Locate every blood parasite and identify its species.
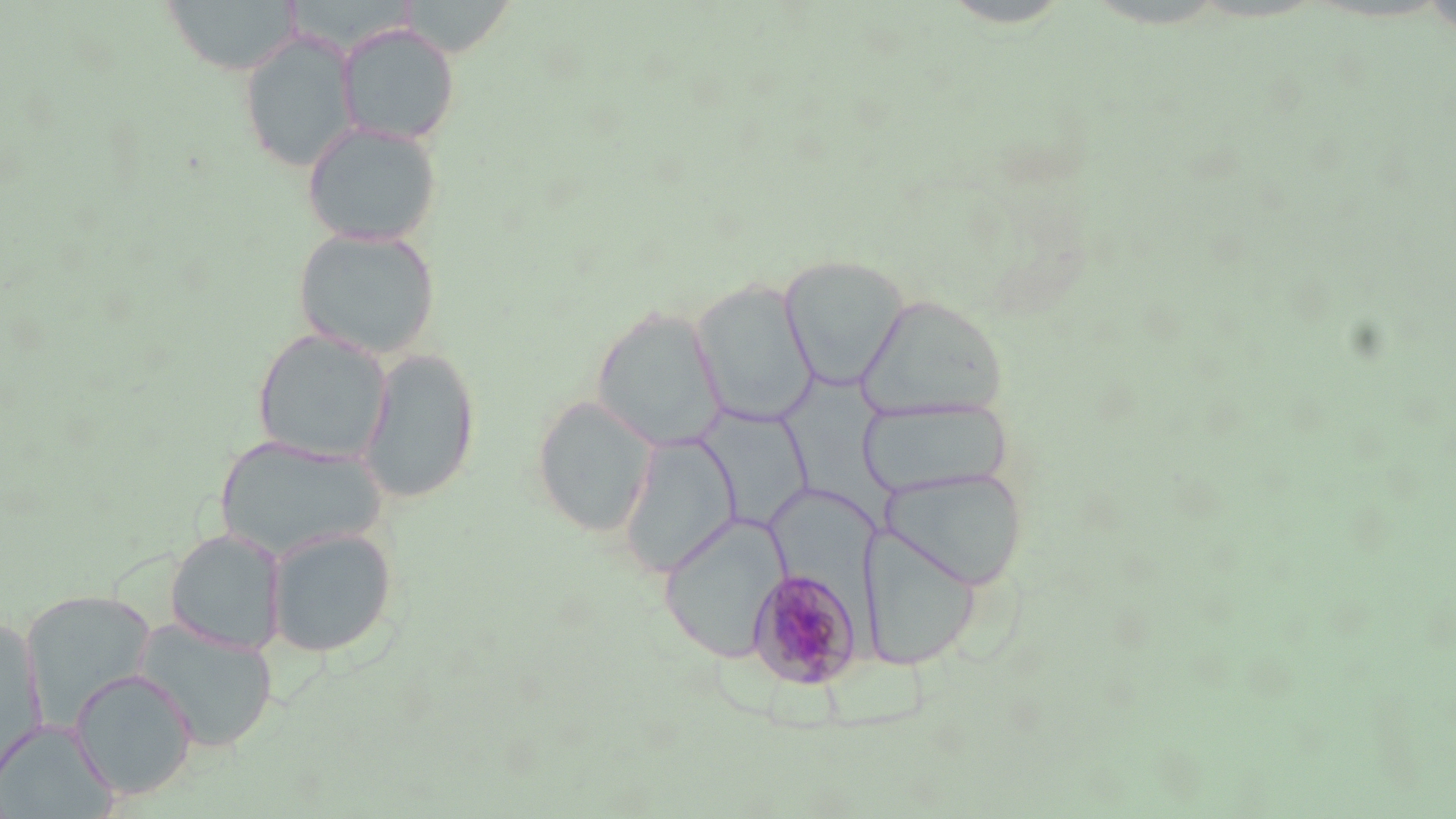
Approximate bounding boxes as (x1, y1, x2, y2) in pixels.
Plasmodium malariae-infected red blood cells: (746, 566, 863, 690).
No Plasmodium falciparum, Plasmodium ovale, Plasmodium vivax, Babesia divergens, or Trypanosoma brucei observed.

slide_level_diagnosis: Plasmodium malariae
preparation: thin blood smear
image_size: 1456×819 pixels
uninfected_red_blood_cell_locations: 'approximate bounding boxes as (x1, y1, x2, y2) in pixels: (161, 0, 301, 76), (336, 22, 461, 147), (238, 30, 359, 173), (301, 120, 444, 248), (292, 226, 442, 359), (779, 253, 909, 391), (691, 279, 819, 428), (855, 292, 1008, 424), (591, 305, 726, 452), (251, 327, 393, 465), (358, 347, 481, 504), (776, 366, 902, 532), (532, 395, 657, 538), (858, 397, 1015, 499), (694, 408, 814, 532), (618, 433, 741, 577), (212, 435, 388, 562), (881, 467, 1028, 591), (658, 515, 787, 663), (859, 522, 982, 671), (265, 525, 399, 659), (165, 528, 286, 657), (21, 590, 157, 727), (132, 618, 279, 753), (0, 619, 47, 785), (69, 668, 197, 800), (0, 719, 119, 819)'
magnification: 1000x
stain: May-Grünwald-Giemsa
field_of_view: single
modality: optical microscopy